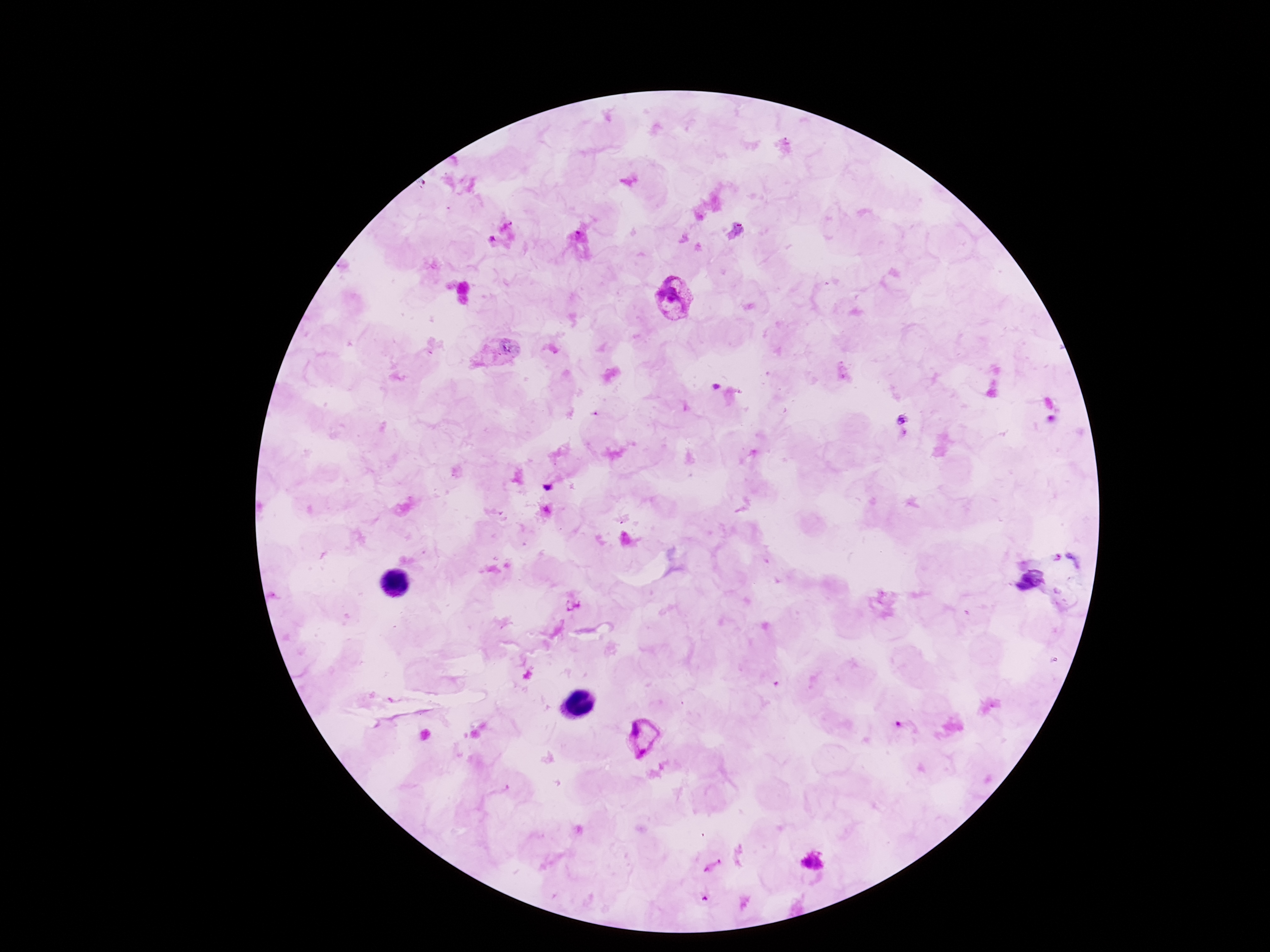

patient malaria status = infected
magnification = 100x
stain = Giemsa
field of view = one from this slide
preparation = thick peripheral-blood smear
capture = smartphone camera through the microscope eyepiece
image size = 1270×952 pixels
Plasmodium parasite locations = approximate centers as (x, y) in pixels: (675, 299), (641, 736), (813, 864)